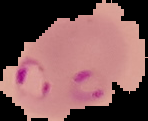

preparation: thin blood smear
malaria_status: parasitized
image_type: segmented cell region on a black background
image_size: 148×121 pixels